Identify the blood parasite species.
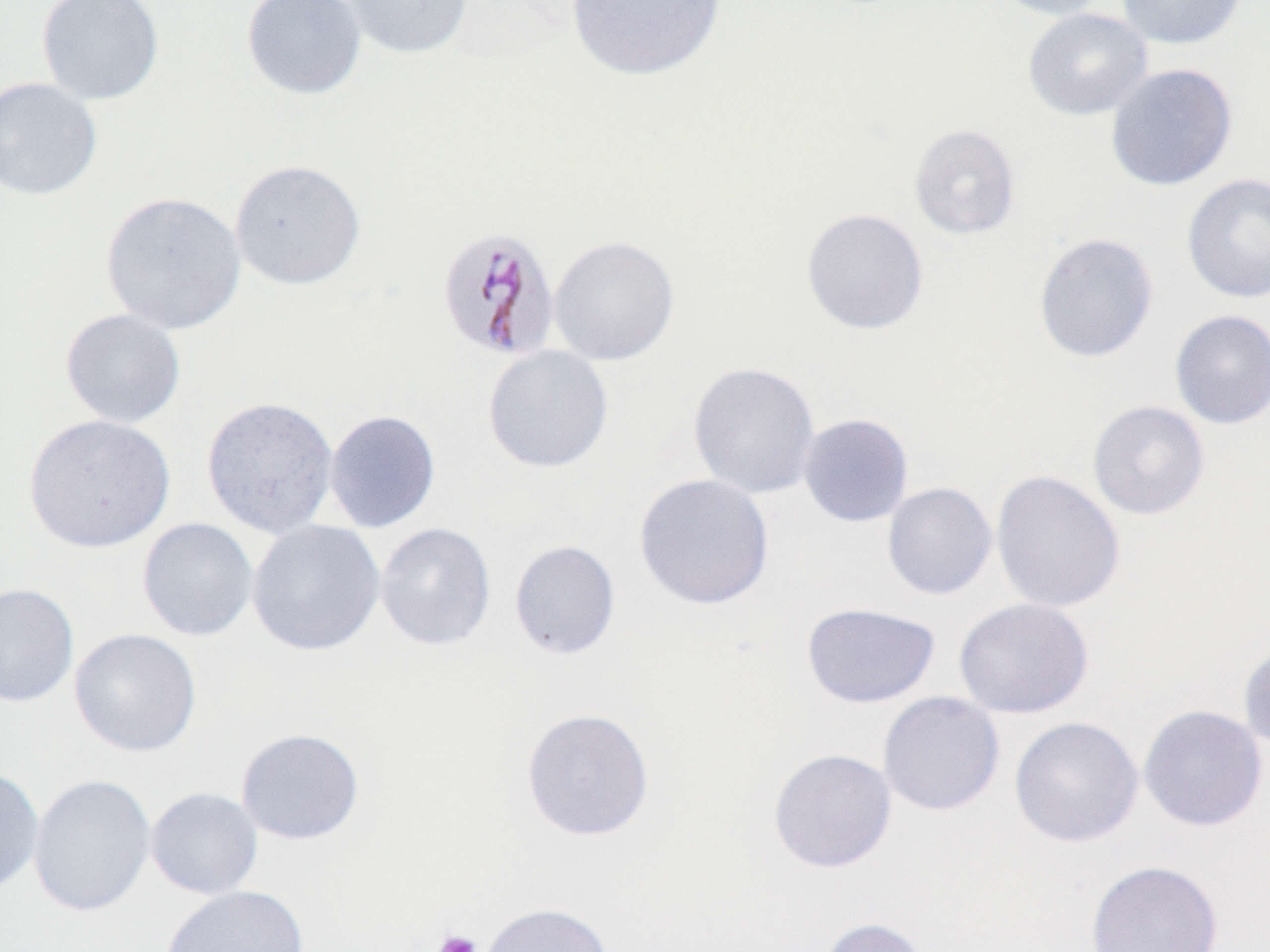

Plasmodium malariae.

Summary:
  - Coordinate format: approximate bounding boxes as (x1,y1)-(x2,y2) corner pairs in pixels
  - Platelet locations: (432,929)-(483,952)
  - Plasmodium malariae-infected red blood cell locations: (435,225)-(561,363)
  - Uninfected red blood cell locations: (35,0)-(165,106), (241,0)-(367,101), (331,0)-(475,60), (565,0)-(727,82), (987,0)-(1115,20), (1116,0)-(1247,50), (1022,8)-(1153,121), (1105,63)-(1237,191), (0,77)-(102,200), (908,124)-(1021,240), (229,159)-(366,291), (1181,173)-(1270,303), (100,191)-(247,335), (800,207)-(929,335), (1033,232)-(1159,363), (548,234)-(680,366), (60,308)-(186,429), (1168,309)-(1270,429), (482,345)-(613,474), (687,361)-(821,499), (200,396)-(339,539), (1087,400)-(1210,520), (324,409)-(441,533), (24,413)-(175,553), (797,413)-(914,528), (990,469)-(1126,613), (634,473)-(774,610), (881,481)-(998,600), (137,518)-(258,641), (246,519)-(386,657), (375,522)-(496,651), (509,540)-(621,659), (0,582)-(79,708), (953,598)-(1094,719), (801,602)-(940,709), (69,628)-(202,757), (1237,637)-(1270,755), (877,691)-(1005,816), (1138,705)-(1268,832), (521,707)-(655,841), (1009,716)-(1143,847), (235,728)-(365,845), (768,748)-(897,873), (0,765)-(45,897), (28,773)-(156,917), (145,787)-(263,900), (1085,859)-(1223,952), (160,884)-(308,952), (480,902)-(614,952), (816,916)-(930,952)
  - Field of view: one of a larger specimen
  - Preparation: thin blood film
  - Stain: May-Grünwald-Giemsa
  - Magnification: 1000x
  - Image size: 1270×952 pixels
  - Modality: light microscopy